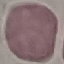

Summary:
  - Malaria status: uninfected
  - Capture: smartphone camera at the microscope eyepiece
  - Stain: Giemsa
  - Image type: cell patch, automatically extracted from a larger field of view and resized to 64 × 64 pixels
  - Preparation: thin blood film